Assess the morphology of the red blood cells.
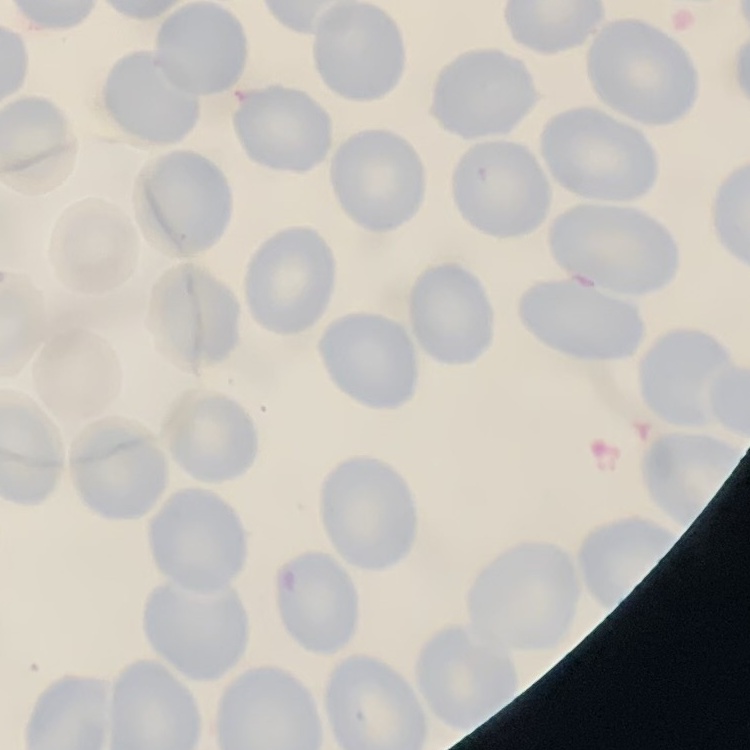
No rouleaux formation.

image type = one tile cut from a larger photomicrograph
stain = Field's or Giemsa
preparation = thin peripheral smear